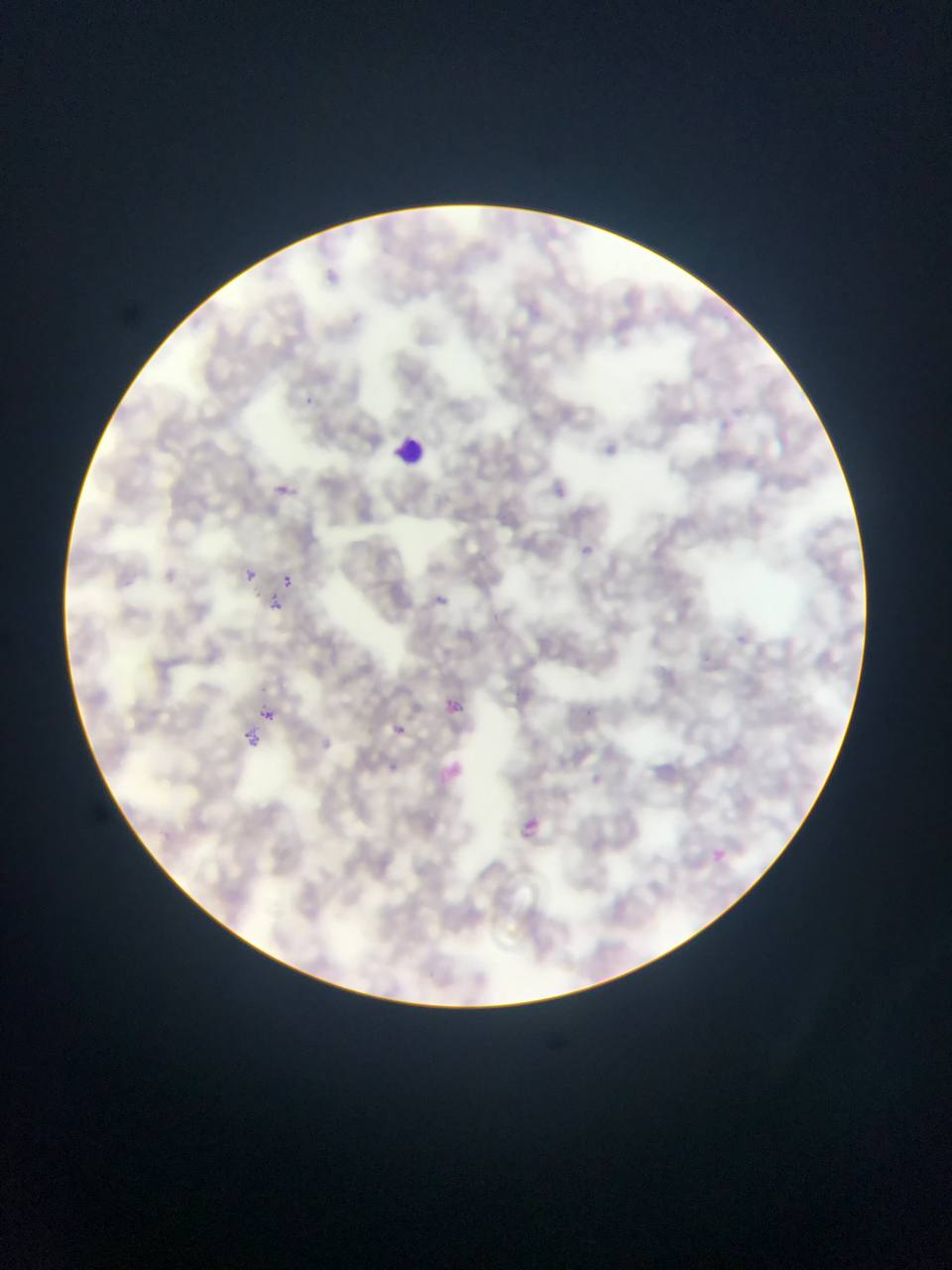

Approximate bounding boxes as left top right bottom in pixels. Leukocyte locations: 391 433 430 472. Plasmodium parasite locations: 306 393 315 409; 269 480 295 501; 578 545 588 553; 244 570 257 581; 281 575 295 589; 432 591 447 605; 264 594 284 614; 440 695 468 723; 258 709 274 726; 384 718 412 743; 243 727 263 750; 432 757 468 795; 388 763 393 773; 511 812 548 846; 707 845 730 866. Image is 952×1270 pixels. One field of view. Thin blood film. Collected in Ghana. Photographed through a microscope with a mobile-phone camera.